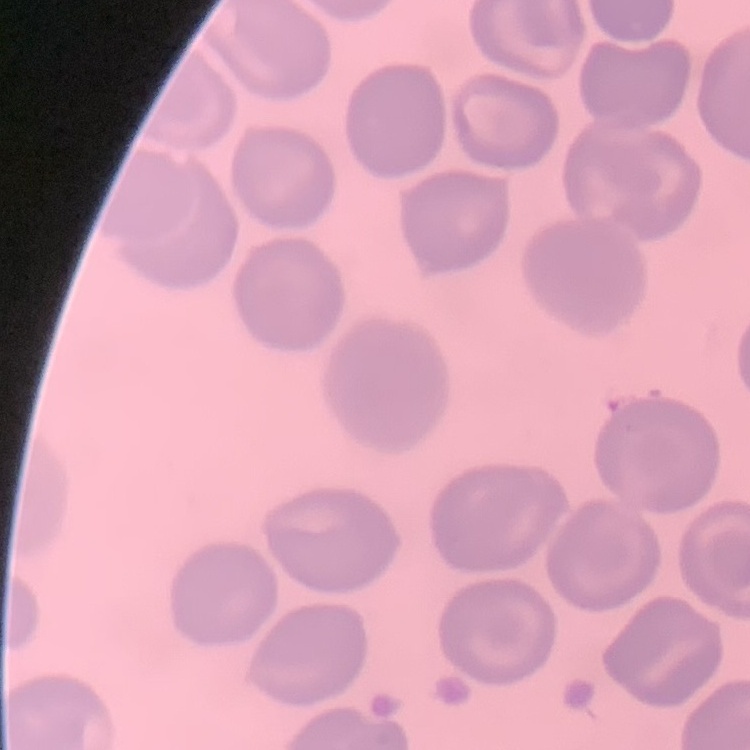

erythrocyte morphology = no rouleaux formation
preparation = thin blood smear
image type = one tile cut from a larger photomicrograph
stain = Field's or Giemsa